Locate every Plasmodium vivax-infected red blood cell.
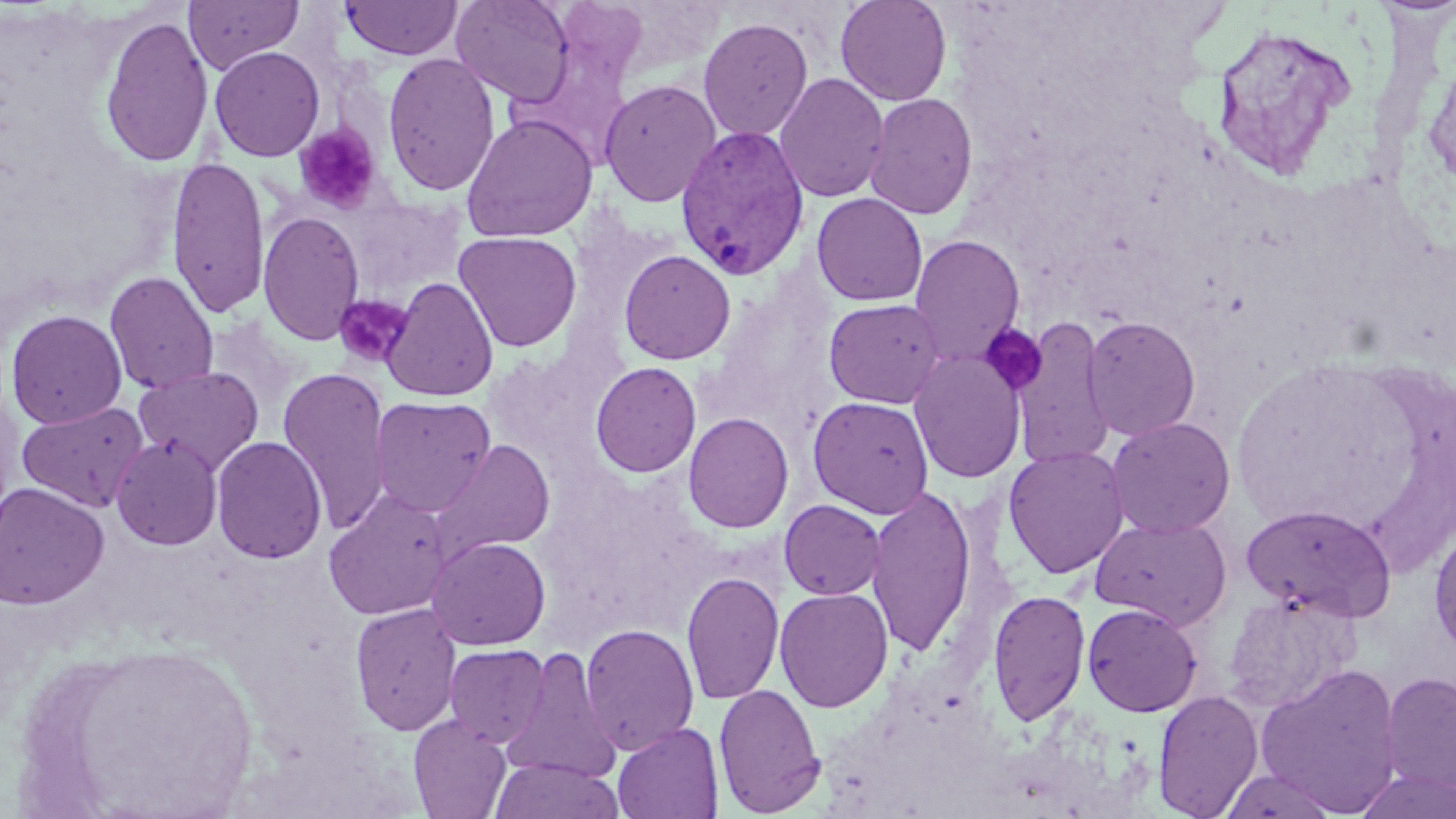
Approximate bounding boxes as (x1, y1, x2, y2) in pixels.
Plasmodium vivax-infected red blood cells: (675, 123, 811, 281).

Summary:
  - Platelet locations: (294, 124, 383, 214), (333, 294, 416, 367), (977, 322, 1047, 396)
  - Uninfected red blood cell locations: (183, 0, 302, 74), (450, 0, 576, 105), (835, 0, 952, 106), (341, 1, 463, 60), (99, 14, 214, 168), (698, 16, 814, 141), (1208, 21, 1362, 182), (1420, 44, 1456, 197), (209, 45, 325, 162), (382, 52, 500, 196), (773, 72, 890, 203), (598, 78, 722, 208), (864, 93, 978, 220), (461, 113, 599, 242), (166, 155, 271, 319), (811, 193, 929, 306), (257, 210, 366, 346), (453, 230, 582, 352), (909, 234, 1026, 364), (619, 249, 736, 365), (104, 271, 219, 394), (382, 277, 499, 401), (823, 298, 946, 408), (5, 309, 128, 429), (1082, 315, 1201, 440), (1011, 316, 1116, 470), (205, 319, 298, 410), (908, 350, 1026, 483), (590, 361, 702, 478), (134, 365, 264, 474), (277, 366, 392, 534), (370, 395, 495, 517), (808, 395, 934, 518), (17, 401, 149, 512), (683, 411, 794, 534), (1105, 416, 1236, 538), (111, 434, 223, 550), (211, 436, 327, 564), (429, 439, 555, 562), (1003, 445, 1129, 578), (0, 482, 109, 609), (866, 483, 977, 656), (323, 491, 453, 621), (779, 498, 886, 600), (1241, 503, 1397, 621), (1090, 516, 1232, 629), (1428, 520, 1456, 660), (426, 535, 551, 650), (681, 570, 784, 705), (774, 587, 894, 712), (987, 588, 1091, 726), (349, 602, 462, 735), (1082, 603, 1202, 717), (580, 623, 700, 756), (34, 635, 266, 816), (444, 644, 550, 747), (499, 648, 623, 785), (1256, 662, 1404, 817), (1380, 670, 1456, 800), (713, 682, 826, 816), (1153, 689, 1263, 818), (408, 714, 512, 818), (613, 722, 724, 819), (489, 757, 625, 819), (1217, 767, 1342, 819), (1353, 769, 1456, 819)
  - Slide-level diagnosis: Plasmodium vivax
  - Image size: 1456×819 pixels
  - Magnification: 1000x
  - Field of view: single
  - Modality: optical microscopy
  - Preparation: thin blood film
  - Stain: May-Grünwald-Giemsa